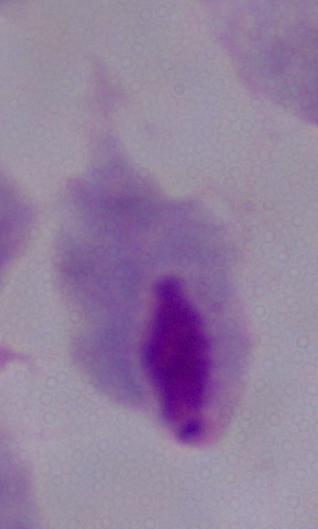
{
  "identification": "trichomonad",
  "magnification": "1000x",
  "modality": "photomicrograph"
}